Outline each blood parasite and name the species.
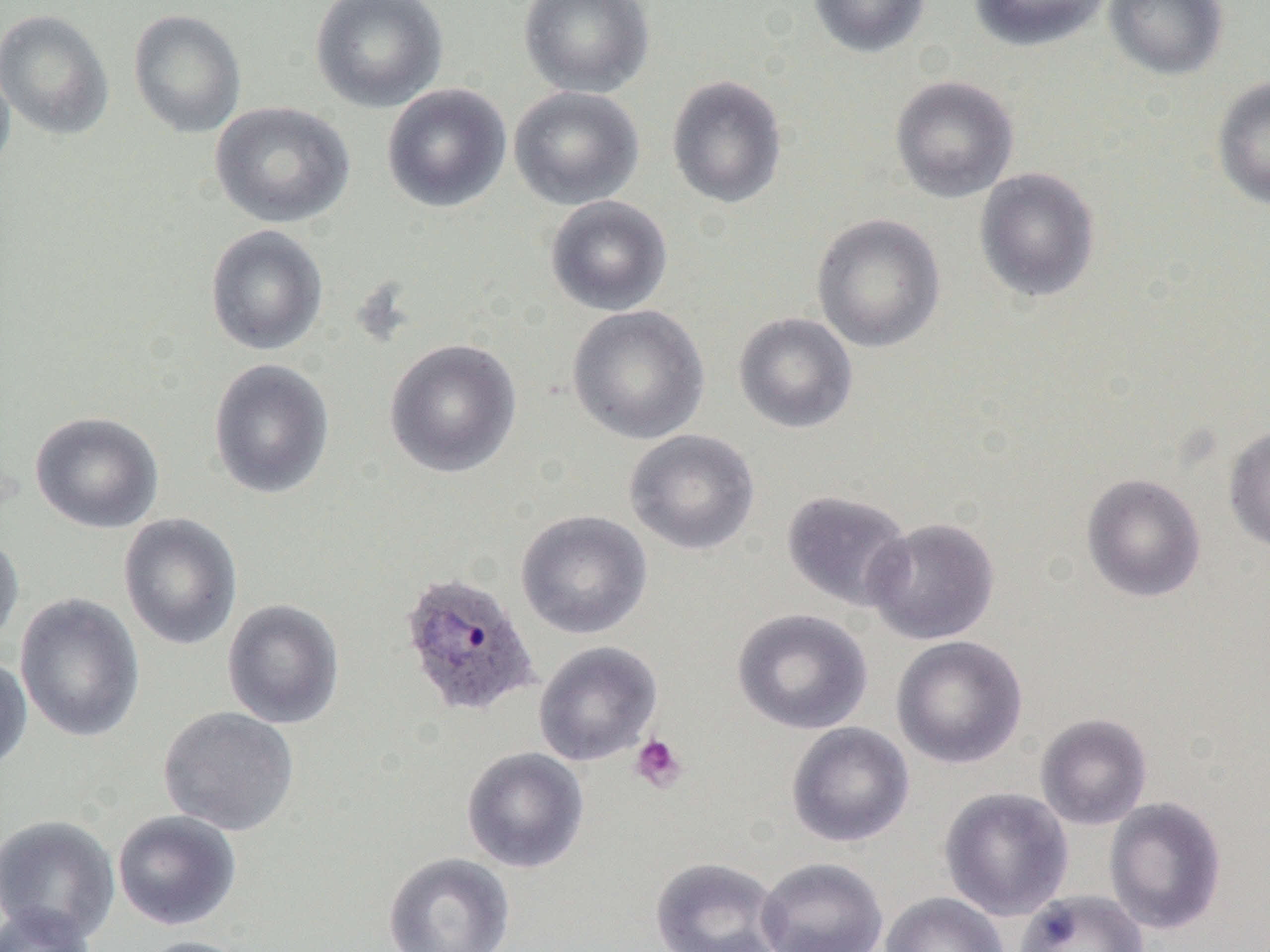
Approximate bounding boxes as (x1,y1)-(x2,y2) corner pairs in pixels.
Plasmodium ovale-infected red blood cells: (398,570)-(541,718).
No Plasmodium falciparum, Plasmodium malariae, Plasmodium vivax, Babesia divergens, or Trypanosoma brucei observed.

slide-level diagnosis = Plasmodium ovale
platelet locations = approximate bounding boxes as (x1,y1)-(x2,y2) corner pairs in pixels: (629,734)-(688,793)
image size = 1270×952 pixels
preparation = thin blood smear
uninfected red blood cell locations = approximate bounding boxes as (x1,y1)-(x2,y2) corner pairs in pixels: (310,0)-(448,112), (519,0)-(655,98), (808,0)-(931,58), (969,0)-(1112,52), (1104,0)-(1228,80), (0,9)-(114,141), (128,9)-(246,138), (0,56)-(16,183), (666,74)-(787,209), (890,75)-(1019,203), (1211,76)-(1270,211), (381,83)-(512,213), (509,85)-(644,210), (209,101)-(355,228), (974,167)-(1101,303), (545,195)-(672,316), (811,213)-(946,353), (204,225)-(328,356), (567,304)-(710,445), (733,312)-(858,434), (384,338)-(522,478), (208,358)-(335,500), (30,411)-(164,534), (1224,426)-(1270,554), (623,429)-(760,556), (1081,472)-(1206,603), (781,489)-(914,612), (515,510)-(652,639), (118,513)-(243,651), (864,517)-(1000,645), (0,530)-(24,652), (14,593)-(145,743), (222,598)-(345,729), (732,608)-(872,735), (891,635)-(1027,769), (534,640)-(662,766), (0,655)-(32,772), (158,706)-(299,836), (1035,713)-(1152,830), (786,722)-(915,847), (461,746)-(590,873), (939,787)-(1073,921), (1103,797)-(1227,935), (112,809)-(242,931), (0,814)-(120,945), (383,851)-(516,952), (649,856)-(787,952), (756,857)-(888,952), (1014,889)-(1149,952), (880,892)-(1009,952), (0,903)-(99,952), (131,935)-(260,952)
magnification = 1000x
field of view = single
modality = light microscopy